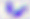

magnification = 400x
modality = photomicrograph
identification = Toxoplasma gondii